Locate and identify every blood parasite.
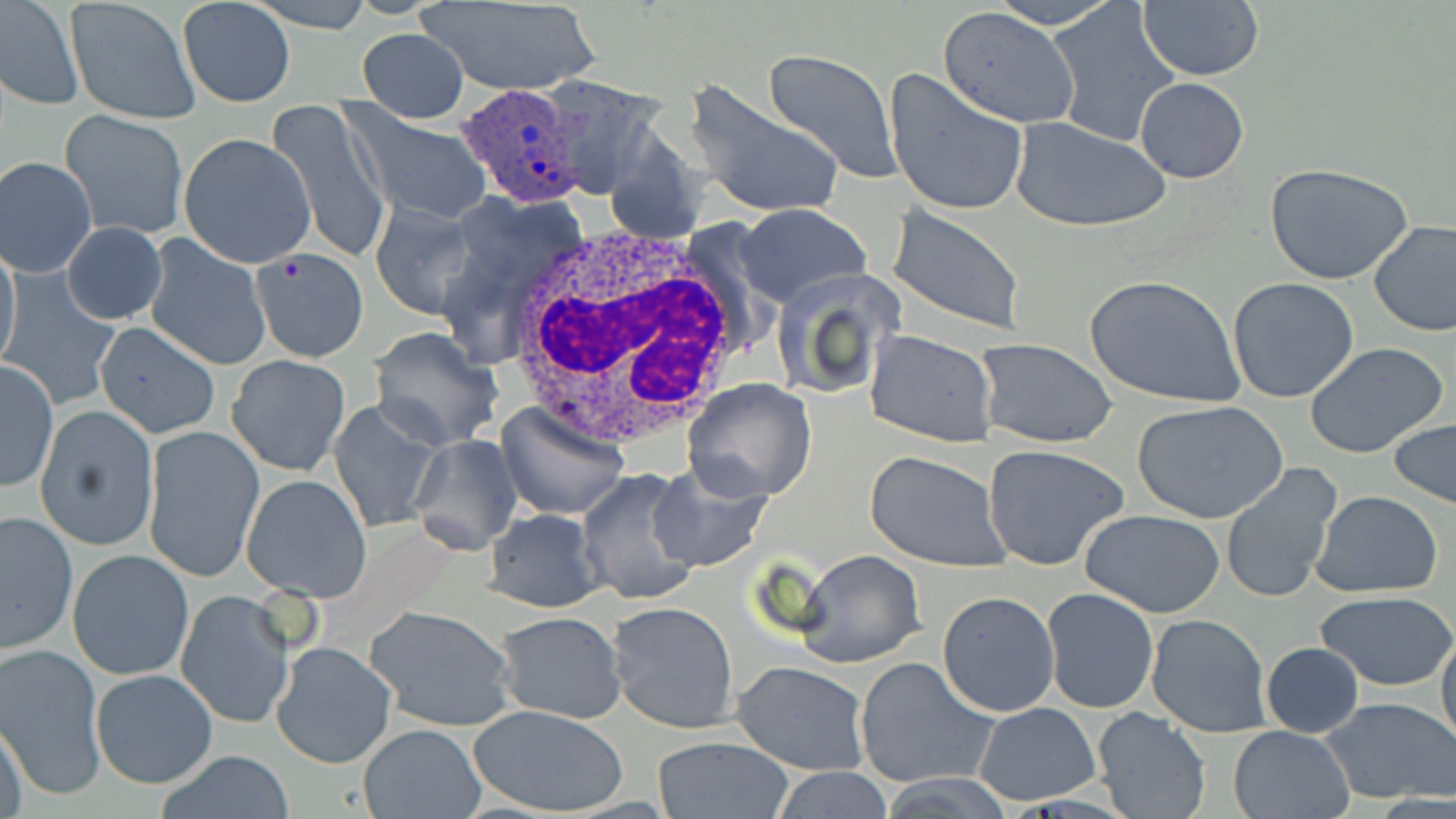

Approximate bounding boxes as (x1,y1)-(x2,y2) corner pairs in pixels.
Plasmodium ovale-infected red blood cells: (455,83)-(586,208).
No Plasmodium falciparum, Plasmodium malariae, Plasmodium vivax, Babesia divergens, or Trypanosoma brucei observed.

Uninfected red blood cell locations: (245,0)-(374,33), (416,0)-(604,96), (986,0)-(1120,29), (67,1)-(200,126), (1138,1)-(1264,83), (1,3)-(81,109), (179,4)-(293,108), (1047,5)-(1181,147), (938,7)-(1079,130), (357,28)-(469,121), (763,48)-(904,185), (883,68)-(1029,217), (537,76)-(663,198), (1134,76)-(1248,183), (683,78)-(846,224), (266,100)-(393,265), (342,107)-(492,224), (61,111)-(188,241), (1010,116)-(1170,234), (179,133)-(316,268), (1,156)-(99,276), (1264,163)-(1413,284), (369,200)-(485,320), (734,203)-(871,310), (884,205)-(1028,336), (1369,219)-(1456,338), (62,221)-(167,325), (143,233)-(271,372), (251,248)-(367,362), (0,249)-(21,371), (769,268)-(904,402), (4,273)-(121,407), (1084,274)-(1246,409), (1227,276)-(1360,402), (92,320)-(221,438), (369,328)-(503,450), (865,328)-(999,449), (975,339)-(1119,450), (1305,343)-(1449,460), (227,354)-(349,476), (1,360)-(58,492), (683,377)-(818,502), (1133,400)-(1288,523), (328,401)-(442,533), (497,403)-(630,522), (35,404)-(158,551), (1388,417)-(1456,509), (143,425)-(263,581), (410,433)-(523,555), (982,443)-(1134,573), (866,450)-(1008,571), (1219,461)-(1343,605), (646,464)-(774,573), (576,467)-(706,609), (241,475)-(372,602), (1311,490)-(1443,597), (0,508)-(79,654), (483,508)-(604,613), (1080,509)-(1226,617), (68,549)-(193,680), (796,549)-(926,669), (1041,588)-(1158,713), (176,590)-(295,730), (1313,590)-(1456,692), (938,592)-(1060,717), (608,600)-(740,733), (365,605)-(515,731), (492,610)-(627,724), (1145,613)-(1272,738), (1436,630)-(1456,751), (271,641)-(398,769), (1261,641)-(1364,737), (0,644)-(106,801), (855,657)-(997,791), (731,661)-(870,777), (90,669)-(217,788), (1319,695)-(1456,806), (975,703)-(1100,805), (470,705)-(629,815), (1093,708)-(1211,819), (0,718)-(30,817), (358,724)-(485,818), (1229,726)-(1354,818), (651,736)-(794,818), (155,750)-(295,819), (766,766)-(895,819). White blood cell locations: (502,224)-(750,450). Slide-level diagnosis: Plasmodium ovale. Image is 1456×819 pixels. Optical microscopy. Thin blood film. 1000x magnification. One field of a larger specimen. May-Grünwald-Giemsa-stained preparation.